State the blood parasite species.
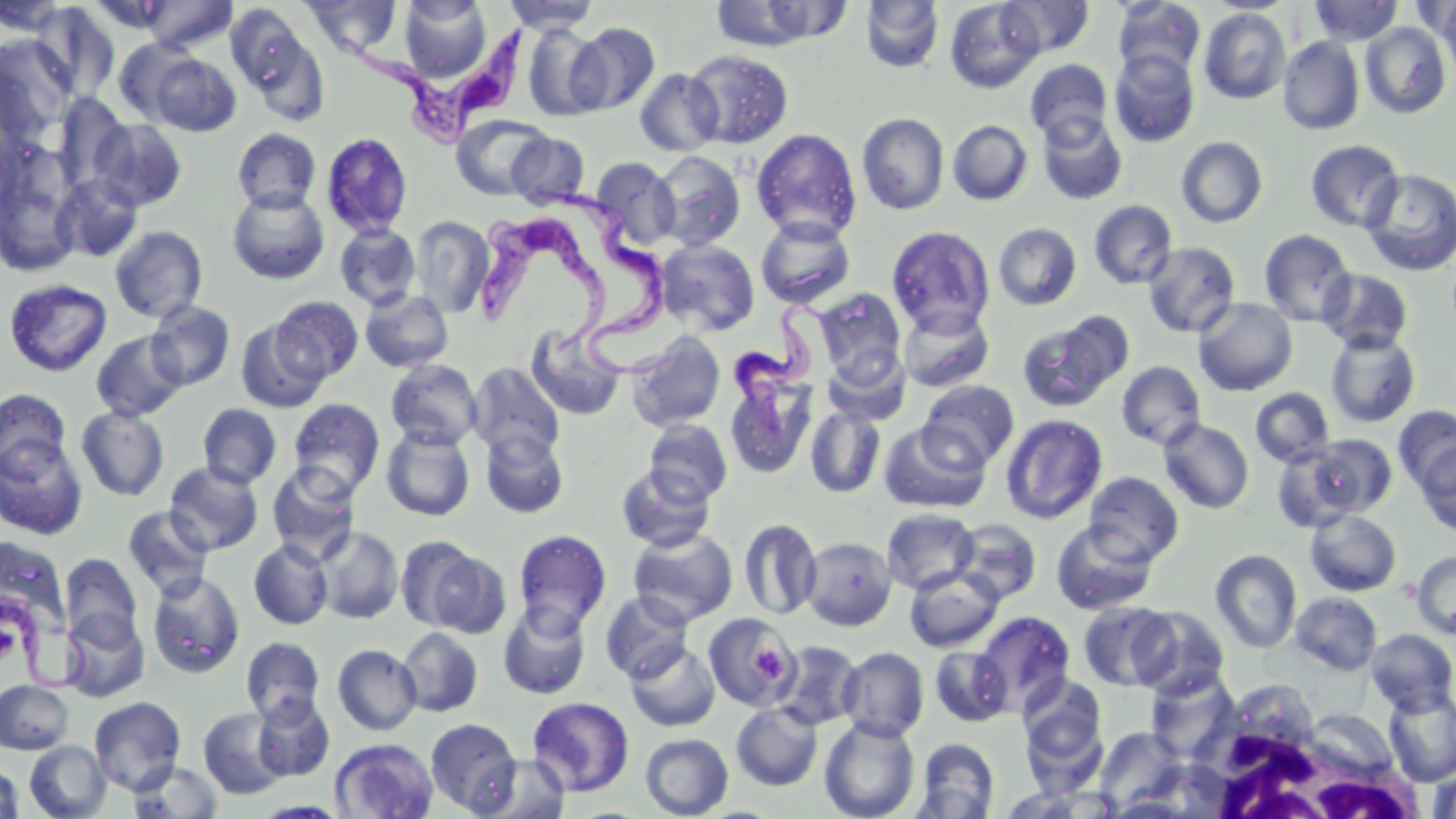

Trypanosoma brucei.

Summary:
  - Coordinate format: approximate bounding boxes as named x1/y1/x2/y2 corners in pixels
  - White blood cell locations: (x1=1188, y1=707, x2=1428, y2=819)
  - Uninfected red blood cell locations: (x1=141, y1=0, x2=238, y2=53), (x1=302, y1=0, x2=402, y2=58), (x1=502, y1=0, x2=601, y2=32), (x1=998, y1=0, x2=1095, y2=58), (x1=1112, y1=0, x2=1206, y2=81), (x1=711, y1=1, x2=843, y2=52), (x1=860, y1=1, x2=945, y2=73), (x1=944, y1=1, x2=1044, y2=94), (x1=1308, y1=1, x2=1403, y2=45), (x1=399, y1=2, x2=491, y2=83), (x1=1437, y1=2, x2=1456, y2=88), (x1=32, y1=3, x2=120, y2=102), (x1=226, y1=5, x2=327, y2=120), (x1=1198, y1=7, x2=1292, y2=105), (x1=568, y1=22, x2=660, y2=115), (x1=1360, y1=22, x2=1452, y2=119), (x1=522, y1=24, x2=609, y2=121), (x1=1277, y1=36, x2=1365, y2=135), (x1=0, y1=37, x2=74, y2=143), (x1=113, y1=38, x2=197, y2=124), (x1=684, y1=49, x2=794, y2=149), (x1=1109, y1=49, x2=1200, y2=148), (x1=148, y1=53, x2=241, y2=136), (x1=1025, y1=59, x2=1113, y2=142), (x1=634, y1=68, x2=724, y2=156), (x1=53, y1=93, x2=132, y2=191), (x1=857, y1=112, x2=949, y2=215), (x1=1036, y1=112, x2=1128, y2=206), (x1=451, y1=114, x2=552, y2=200), (x1=90, y1=119, x2=187, y2=211), (x1=947, y1=120, x2=1033, y2=206), (x1=231, y1=128, x2=321, y2=213), (x1=751, y1=128, x2=862, y2=243), (x1=321, y1=131, x2=414, y2=238), (x1=507, y1=132, x2=590, y2=209), (x1=1176, y1=136, x2=1268, y2=228), (x1=1305, y1=139, x2=1405, y2=233), (x1=651, y1=151, x2=746, y2=251), (x1=591, y1=156, x2=681, y2=249), (x1=1359, y1=168, x2=1456, y2=276), (x1=0, y1=169, x2=80, y2=278), (x1=52, y1=173, x2=145, y2=262), (x1=226, y1=188, x2=330, y2=285), (x1=1088, y1=200, x2=1178, y2=289), (x1=409, y1=215, x2=495, y2=318), (x1=755, y1=217, x2=856, y2=309), (x1=334, y1=223, x2=422, y2=310), (x1=993, y1=223, x2=1083, y2=310), (x1=886, y1=225, x2=995, y2=335), (x1=110, y1=226, x2=208, y2=323), (x1=1258, y1=229, x2=1356, y2=326), (x1=655, y1=239, x2=760, y2=335), (x1=1142, y1=242, x2=1241, y2=338), (x1=1317, y1=269, x2=1414, y2=354), (x1=4, y1=278, x2=112, y2=377), (x1=360, y1=289, x2=455, y2=372), (x1=813, y1=289, x2=906, y2=381), (x1=270, y1=296, x2=363, y2=383), (x1=1192, y1=297, x2=1298, y2=396), (x1=147, y1=301, x2=236, y2=391), (x1=897, y1=304, x2=995, y2=392), (x1=1016, y1=313, x2=1130, y2=412), (x1=235, y1=319, x2=329, y2=412), (x1=523, y1=323, x2=626, y2=422), (x1=90, y1=330, x2=188, y2=421), (x1=1325, y1=330, x2=1421, y2=428), (x1=626, y1=331, x2=726, y2=432), (x1=823, y1=349, x2=909, y2=426), (x1=386, y1=359, x2=483, y2=451), (x1=469, y1=361, x2=565, y2=462), (x1=1116, y1=361, x2=1206, y2=450), (x1=724, y1=367, x2=818, y2=480), (x1=919, y1=380, x2=1019, y2=468), (x1=0, y1=388, x2=72, y2=476), (x1=1250, y1=388, x2=1334, y2=467), (x1=288, y1=398, x2=386, y2=499), (x1=197, y1=403, x2=282, y2=488), (x1=805, y1=405, x2=886, y2=499), (x1=1393, y1=405, x2=1456, y2=494), (x1=76, y1=406, x2=169, y2=501), (x1=1001, y1=415, x2=1107, y2=524), (x1=644, y1=419, x2=732, y2=505), (x1=1159, y1=419, x2=1254, y2=514), (x1=877, y1=422, x2=991, y2=513), (x1=381, y1=426, x2=476, y2=521), (x1=480, y1=428, x2=569, y2=518), (x1=0, y1=435, x2=88, y2=541), (x1=1272, y1=442, x2=1372, y2=532), (x1=1414, y1=443, x2=1455, y2=536), (x1=164, y1=461, x2=264, y2=556), (x1=266, y1=462, x2=361, y2=562), (x1=616, y1=463, x2=716, y2=552), (x1=1084, y1=472, x2=1184, y2=565), (x1=122, y1=506, x2=214, y2=599), (x1=881, y1=508, x2=980, y2=594), (x1=1305, y1=509, x2=1402, y2=596), (x1=951, y1=517, x2=1043, y2=605), (x1=738, y1=519, x2=822, y2=620), (x1=1051, y1=520, x2=1158, y2=616), (x1=316, y1=526, x2=404, y2=624), (x1=628, y1=527, x2=738, y2=625), (x1=513, y1=529, x2=612, y2=633), (x1=395, y1=535, x2=492, y2=633), (x1=0, y1=536, x2=71, y2=634), (x1=802, y1=536, x2=897, y2=631), (x1=249, y1=539, x2=333, y2=630), (x1=1210, y1=549, x2=1302, y2=653), (x1=1411, y1=550, x2=1456, y2=640), (x1=59, y1=553, x2=143, y2=647), (x1=904, y1=567, x2=1003, y2=652), (x1=147, y1=571, x2=246, y2=678), (x1=599, y1=590, x2=694, y2=684), (x1=1290, y1=592, x2=1383, y2=674), (x1=497, y1=602, x2=591, y2=699), (x1=1078, y1=602, x2=1176, y2=691), (x1=1130, y1=606, x2=1230, y2=699), (x1=59, y1=609, x2=149, y2=702), (x1=974, y1=611, x2=1075, y2=714), (x1=702, y1=612, x2=800, y2=711), (x1=397, y1=627, x2=483, y2=717), (x1=1366, y1=629, x2=1456, y2=714), (x1=241, y1=637, x2=326, y2=723), (x1=771, y1=640, x2=864, y2=731), (x1=625, y1=641, x2=721, y2=732), (x1=332, y1=643, x2=422, y2=735), (x1=929, y1=646, x2=1014, y2=727), (x1=838, y1=647, x2=929, y2=741), (x1=927, y1=647, x2=1009, y2=817), (x1=1146, y1=670, x2=1238, y2=761), (x1=1018, y1=675, x2=1109, y2=775), (x1=0, y1=680, x2=74, y2=754), (x1=1383, y1=688, x2=1456, y2=786), (x1=252, y1=694, x2=335, y2=781), (x1=89, y1=696, x2=187, y2=795), (x1=527, y1=697, x2=635, y2=797), (x1=730, y1=702, x2=823, y2=791), (x1=198, y1=707, x2=289, y2=799), (x1=1306, y1=708, x2=1399, y2=781), (x1=818, y1=716, x2=920, y2=819), (x1=425, y1=717, x2=522, y2=815), (x1=1095, y1=727, x2=1186, y2=810), (x1=639, y1=733, x2=733, y2=818), (x1=330, y1=737, x2=439, y2=819), (x1=915, y1=738, x2=1000, y2=818), (x1=24, y1=741, x2=111, y2=818), (x1=471, y1=754, x2=572, y2=818), (x1=128, y1=761, x2=223, y2=819), (x1=0, y1=764, x2=23, y2=818), (x1=1428, y1=768, x2=1456, y2=819), (x1=999, y1=784, x2=1113, y2=818)
  - Trypanosoma brucei locations: (x1=336, y1=13, x2=539, y2=149), (x1=554, y1=185, x2=706, y2=387), (x1=476, y1=219, x2=606, y2=355), (x1=732, y1=299, x2=842, y2=446), (x1=0, y1=594, x2=99, y2=694)
  - Platelet locations: (x1=752, y1=643, x2=787, y2=678)
  - Image size: 1456×819 pixels
  - Preparation: thin blood film
  - Field of view: single
  - Magnification: 1000x
  - Stain: May-Grünwald-Giemsa
  - Modality: optical microscopy